State which parasite is depicted.
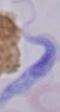

A trypanosome.

magnification = 1000x
modality = micrograph